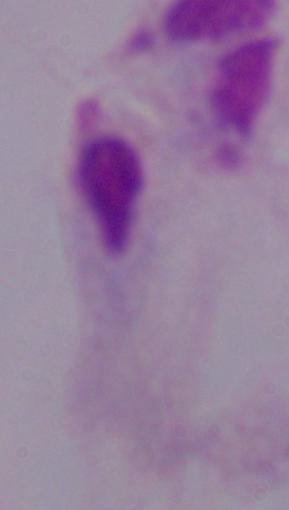

magnification = 1000x
identification = trichomonad
modality = micrograph